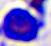
Summary:
  - Magnification: 400x
  - Modality: photomicrograph
  - Identification: white blood cell